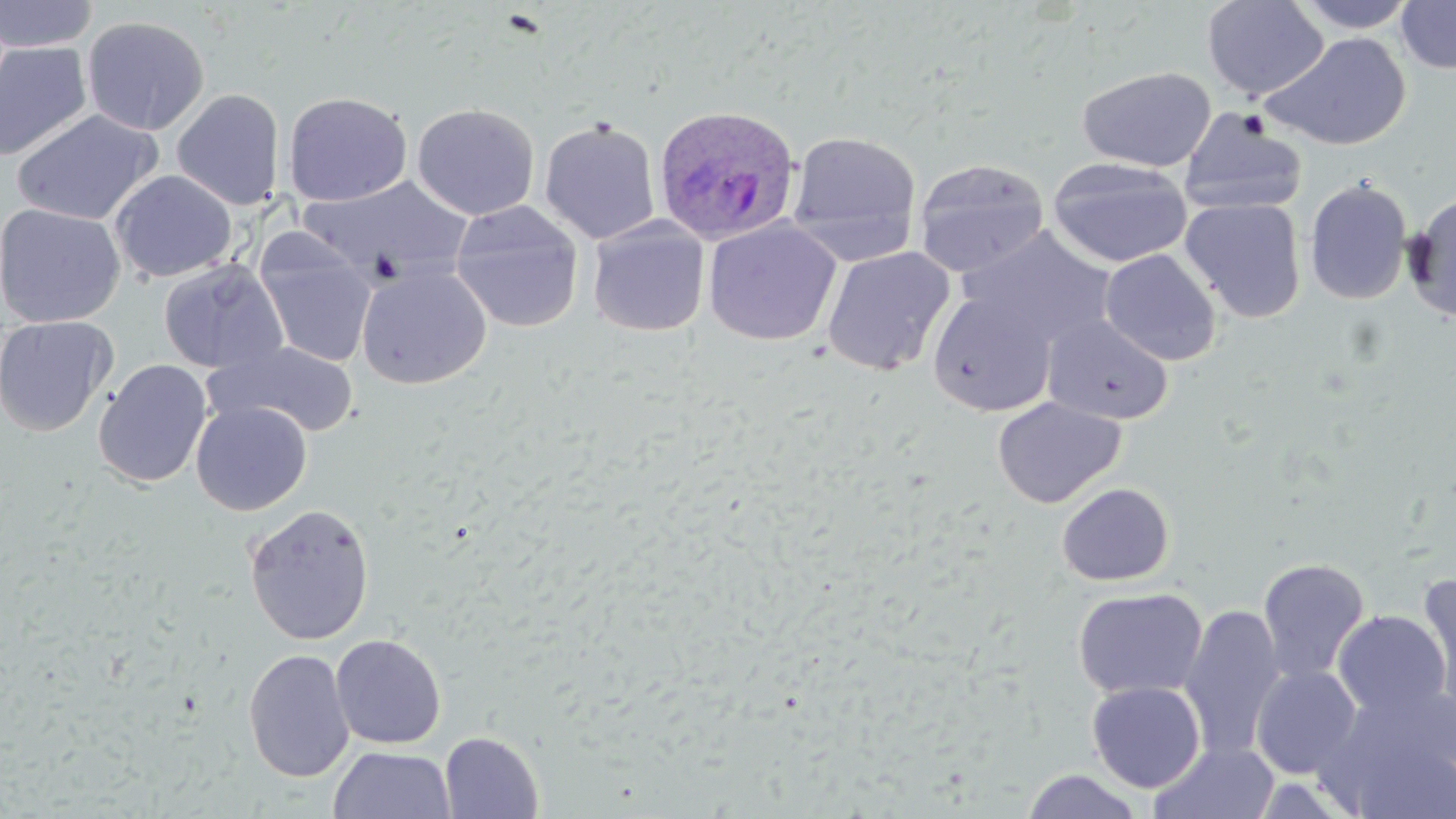

slide_level_diagnosis: Plasmodium ovale
preparation: thin blood smear
modality: optical microscopy
plasmodium_ovale_infected_red_blood_cell_locations: 'approximate bounding boxes as named x1/y1/x2/y2 corners in pixels: (x1=652, y1=103, x2=801, y2=246)'
magnification: 1000x
stain: May-Grünwald-Giemsa
image_size: 1456×819 pixels
uninfected_red_blood_cell_locations: 'approximate bounding boxes as named x1/y1/x2/y2 corners in pixels: (x1=0, y1=0, x2=98, y2=53), (x1=1201, y1=0, x2=1328, y2=100), (x1=1293, y1=0, x2=1419, y2=33), (x1=1396, y1=0, x2=1456, y2=73), (x1=81, y1=15, x2=210, y2=136), (x1=1263, y1=32, x2=1412, y2=151), (x1=0, y1=41, x2=93, y2=161), (x1=1077, y1=65, x2=1216, y2=172), (x1=172, y1=88, x2=285, y2=210), (x1=283, y1=91, x2=412, y2=207), (x1=411, y1=103, x2=540, y2=220), (x1=11, y1=108, x2=163, y2=225), (x1=1179, y1=109, x2=1308, y2=216), (x1=539, y1=118, x2=661, y2=245), (x1=786, y1=130, x2=922, y2=262), (x1=1047, y1=157, x2=1193, y2=268), (x1=913, y1=158, x2=1050, y2=277), (x1=110, y1=169, x2=237, y2=283), (x1=297, y1=176, x2=472, y2=284), (x1=1303, y1=178, x2=1413, y2=306), (x1=1403, y1=192, x2=1456, y2=323), (x1=1181, y1=197, x2=1306, y2=323), (x1=448, y1=200, x2=585, y2=333), (x1=0, y1=203, x2=125, y2=327), (x1=587, y1=218, x2=710, y2=337), (x1=703, y1=219, x2=842, y2=346), (x1=963, y1=228, x2=1115, y2=347), (x1=254, y1=236, x2=377, y2=368), (x1=820, y1=246, x2=955, y2=377), (x1=1100, y1=248, x2=1221, y2=365), (x1=157, y1=258, x2=288, y2=374), (x1=356, y1=264, x2=492, y2=389), (x1=928, y1=290, x2=1056, y2=416), (x1=1043, y1=314, x2=1174, y2=425), (x1=0, y1=315, x2=117, y2=436), (x1=208, y1=340, x2=359, y2=438), (x1=93, y1=359, x2=212, y2=488), (x1=992, y1=397, x2=1126, y2=508), (x1=191, y1=401, x2=311, y2=516), (x1=1056, y1=482, x2=1175, y2=586), (x1=243, y1=503, x2=376, y2=645), (x1=1258, y1=557, x2=1371, y2=683), (x1=1415, y1=575, x2=1456, y2=710), (x1=1072, y1=587, x2=1207, y2=700), (x1=1179, y1=605, x2=1285, y2=760), (x1=1333, y1=610, x2=1452, y2=720), (x1=330, y1=633, x2=447, y2=749), (x1=243, y1=649, x2=355, y2=783), (x1=1251, y1=665, x2=1362, y2=778), (x1=1086, y1=681, x2=1206, y2=793), (x1=1319, y1=686, x2=1456, y2=817), (x1=440, y1=731, x2=544, y2=819), (x1=1149, y1=741, x2=1280, y2=819), (x1=328, y1=746, x2=456, y2=819), (x1=1020, y1=769, x2=1146, y2=818)'
field_of_view: one of a larger specimen